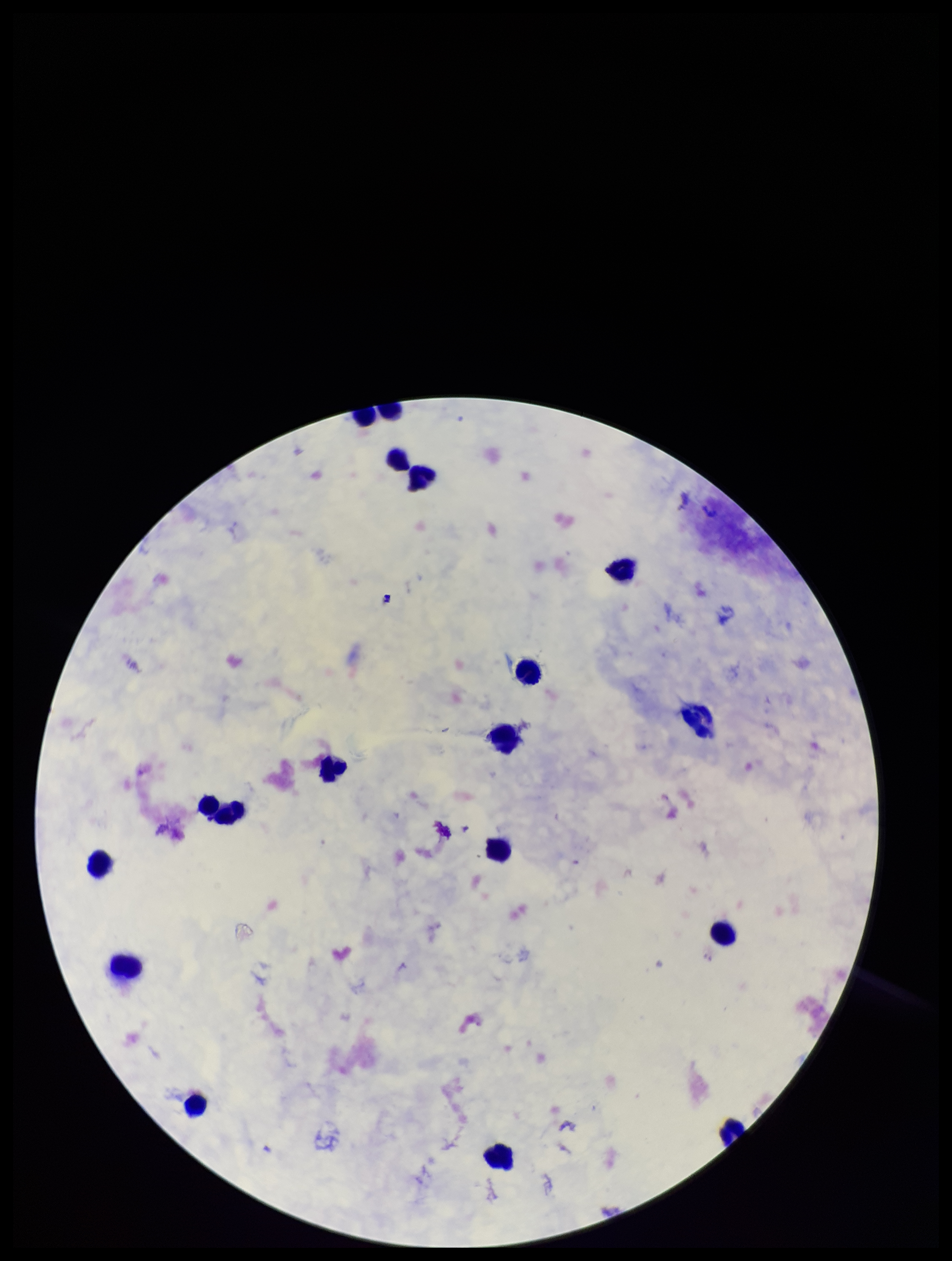
Summary:
  - Image size: 952×1261 pixels
  - Preparation: thick
  - Parasite count: 0
  - Leukocyte count: 16
  - Capture: smartphone photograph through the microscope eyepiece
  - Species reported for this patient: Plasmodium falciparum
  - Patient malaria status: positive
  - Plasmodium parasites: none identified
  - Stain: Giemsa
  - Field of view: one from this slide